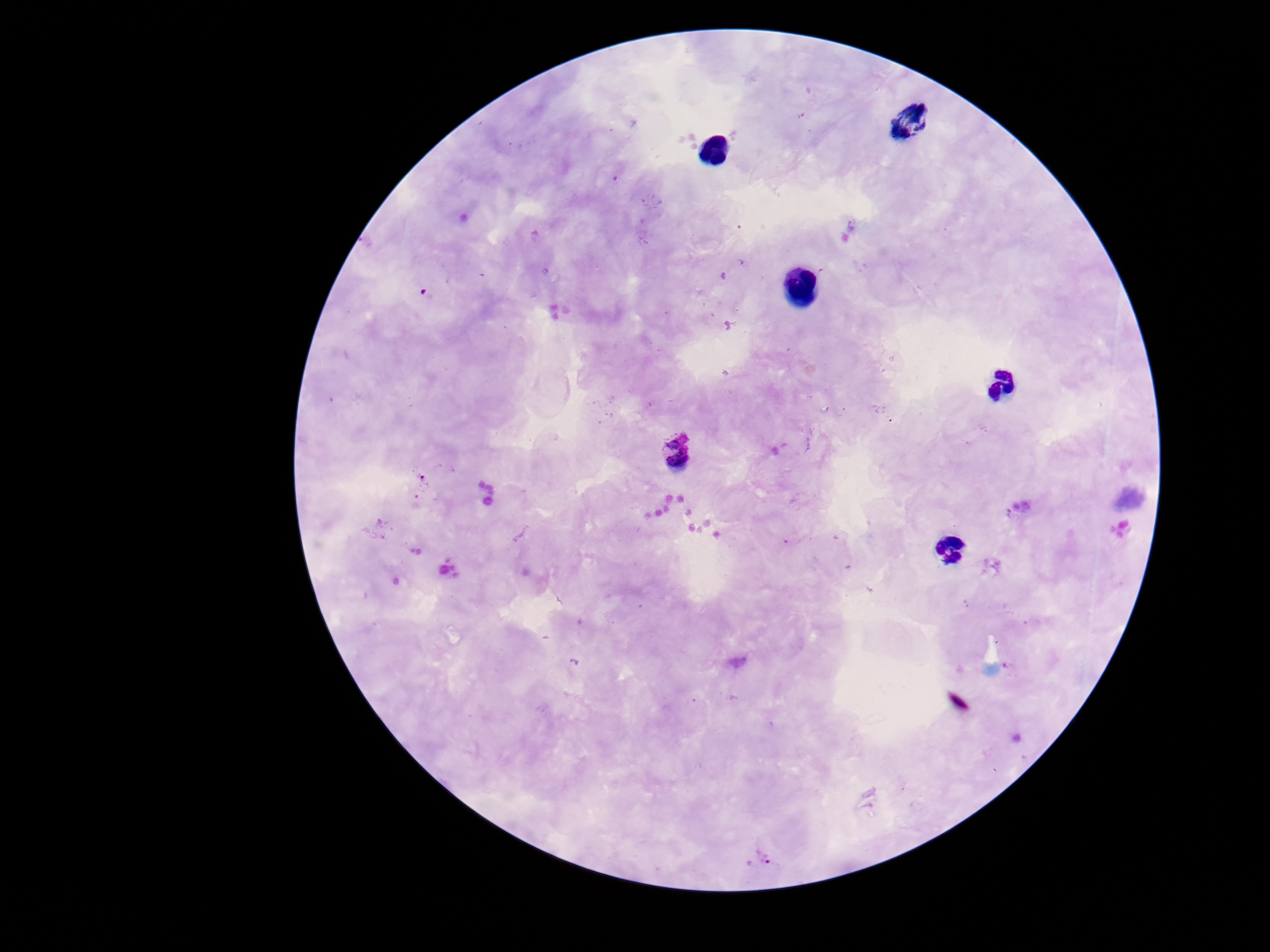
Approximate centers as {x, y} in pixels.
Summary:
  - Plasmodium parasite locations: {678, 452}, {761, 858}
  - Capture: smartphone camera through the microscope eyepiece
  - Magnification: 100x
  - Preparation: thick peripheral-blood smear
  - Patient malaria status: positive
  - Stain: Giemsa
  - Field of view: single
  - Image size: 1270×952 pixels